Name the blood parasite species.
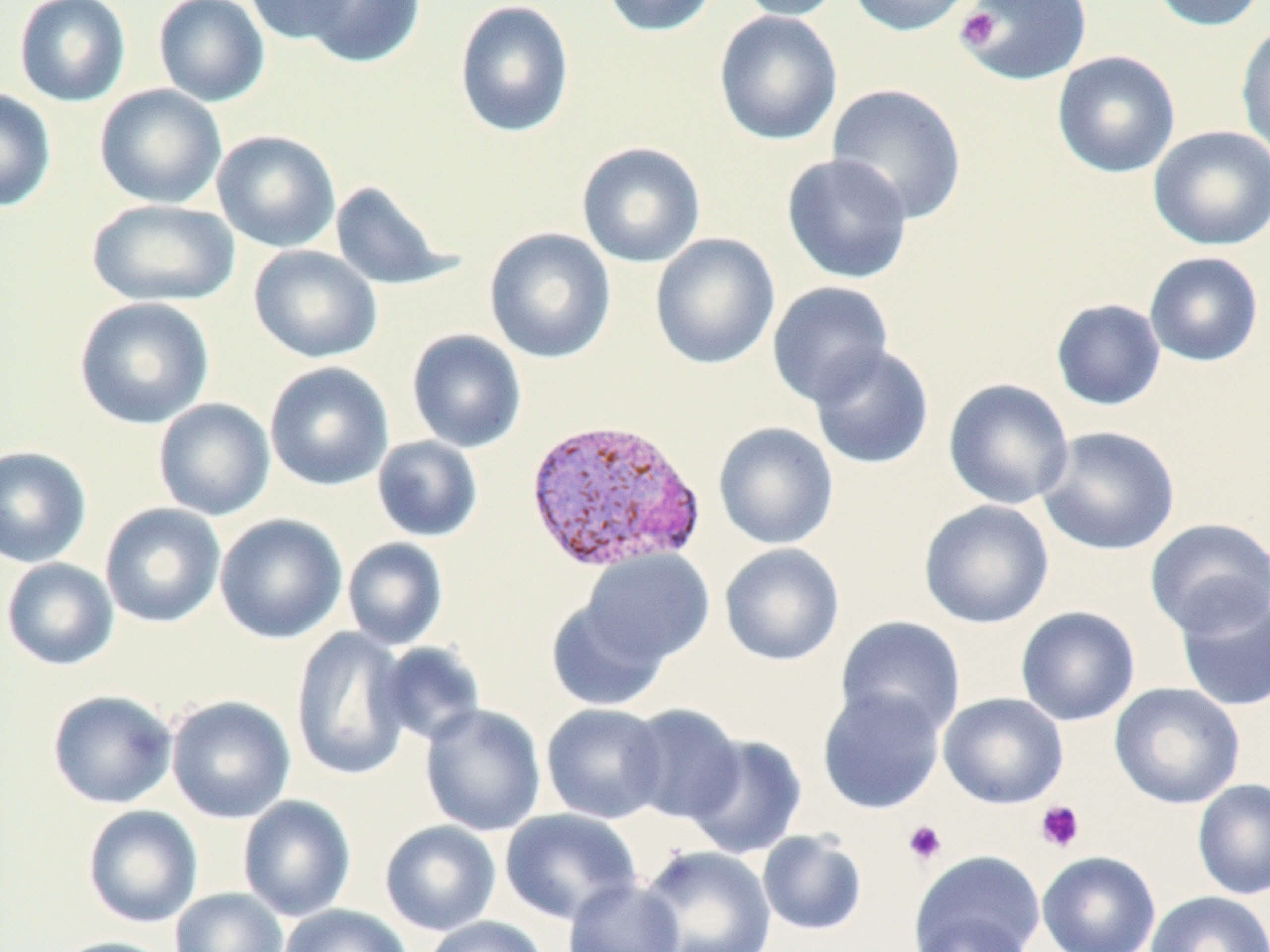

Plasmodium vivax.

Approximate bounding boxes as (x1,y1)-(x2,y2) corner pairs in pixels. Uninfected red blood cell locations: (13,0)-(131,107), (152,0)-(270,107), (244,0)-(360,46), (298,0)-(427,69), (454,0)-(575,138), (599,0)-(719,37), (731,0)-(846,21), (847,0)-(977,37), (958,0)-(1093,86), (1147,0)-(1267,32), (713,10)-(844,146), (1235,22)-(1270,162), (1052,50)-(1181,178), (826,83)-(968,224), (94,84)-(227,209), (0,89)-(57,213), (1148,125)-(1270,251), (211,130)-(341,253), (576,141)-(706,268), (781,153)-(913,284), (330,181)-(457,291), (87,199)-(240,307), (484,227)-(617,364), (649,232)-(781,370), (248,245)-(383,364), (1144,252)-(1264,367), (766,281)-(895,408), (73,296)-(216,430), (1050,298)-(1167,411), (406,329)-(527,453), (808,344)-(935,470), (264,361)-(394,491), (943,378)-(1075,509), (153,398)-(275,521), (713,422)-(839,550), (1036,425)-(1181,556), (372,436)-(483,542), (0,446)-(92,568), (918,500)-(1054,629), (99,503)-(226,628), (214,513)-(347,644), (1145,518)-(1270,637), (342,538)-(449,650), (719,543)-(845,666), (579,548)-(715,668), (1,557)-(119,671), (1173,587)-(1270,712), (545,598)-(669,712), (1015,606)-(1141,726), (835,616)-(966,739), (289,628)-(413,781), (377,641)-(486,746), (1108,682)-(1246,810), (817,686)-(946,815), (47,689)-(178,809), (938,692)-(1069,809), (166,695)-(296,824), (541,702)-(670,824), (419,703)-(546,837), (622,704)-(745,825), (684,734)-(807,859), (1192,778)-(1270,900), (237,795)-(356,922), (82,805)-(203,928), (500,808)-(642,924), (379,820)-(502,936), (756,829)-(869,936), (638,845)-(777,952), (908,850)-(1045,952), (1037,850)-(1161,952), (562,877)-(685,952), (169,887)-(288,952), (1145,891)-(1270,952), (279,903)-(412,952), (908,913)-(1039,952), (420,915)-(548,952), (47,936)-(178,952). Platelet locations: (956,7)-(1003,52), (1035,800)-(1084,852), (903,820)-(947,865). Plasmodium vivax-infected red blood cell locations: (522,415)-(707,574). 1000x magnification. Thin blood film. Image is 1270×952 pixels. One field of a larger specimen. May-Grünwald-Giemsa stain. Optical microscopy.